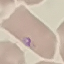
Summary:
  - Malaria status: parasitized
  - Image type: automatically extracted cell patch, resized to 64 × 64 pixels
  - Stain: Giemsa
  - Capture: smartphone camera at the microscope eyepiece
  - Preparation: thin smear